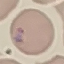
{
  "malaria_status": "parasitized",
  "preparation": "thin blood film",
  "stain": "Giemsa",
  "capture": "smartphone camera at the microscope eyepiece",
  "image_type": "cell patch, automatically extracted from a larger field of view and resized to 64 × 64 pixels"
}